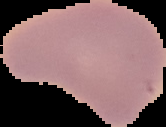

Summary:
  - Image size: 166×127 pixels
  - Image type: segmented cell region with the area outside set to black
  - Preparation: thin blood smear
  - Malaria status: uninfected